State which parasite is depicted.
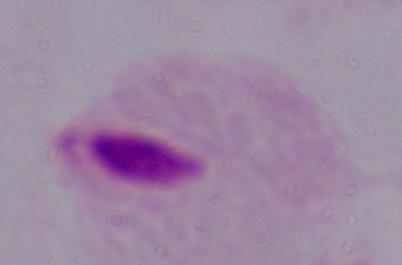
This is a trichomonad.

Summary:
  - Modality: micrograph
  - Magnification: 1000x